Identify the preparation type.
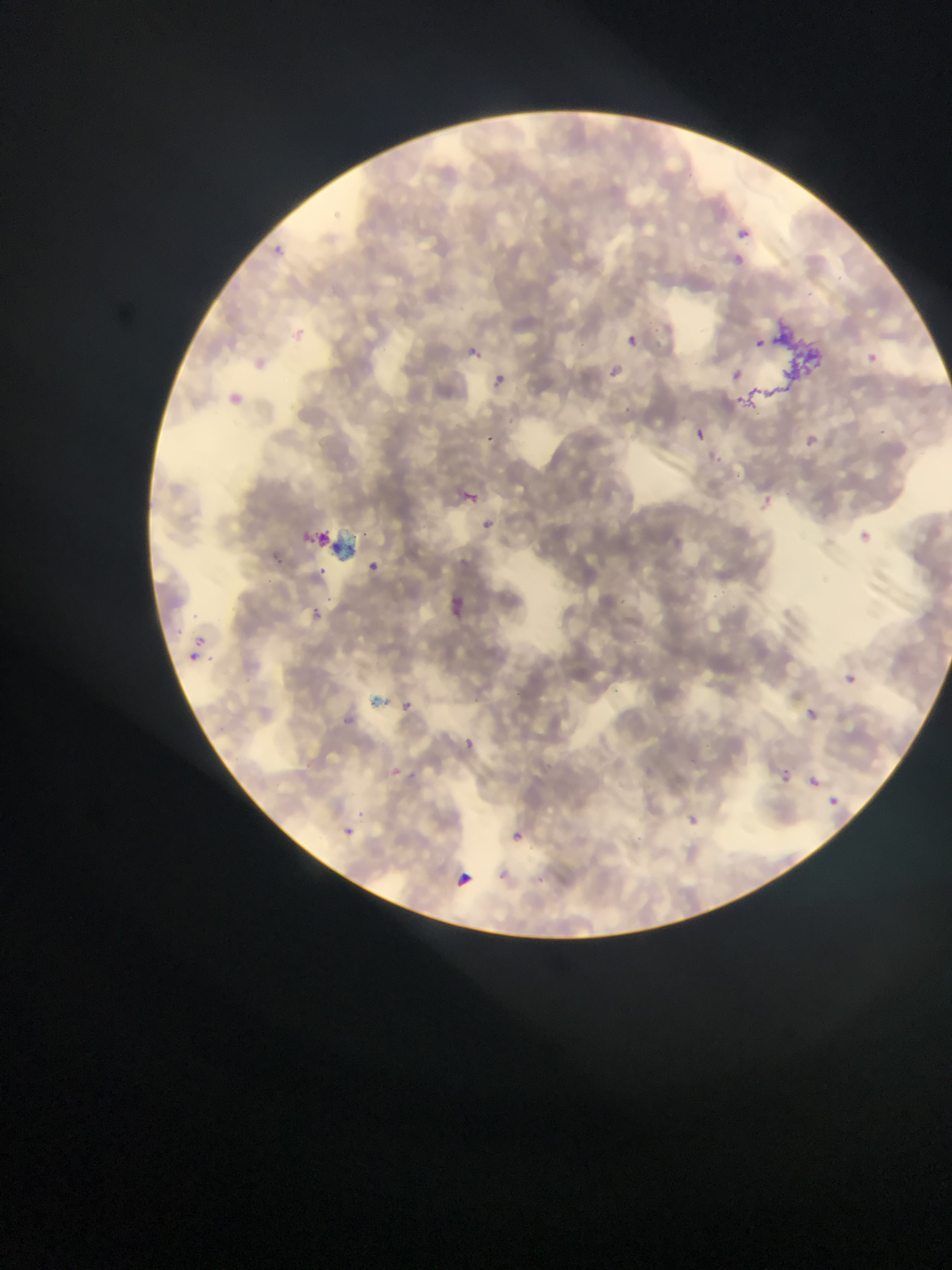

This is a thin smear.

country = Ghana
field of view = single
image size = 952×1270 pixels
capture = mobile-phone photograph through a microscope
malaria parasite locations = approximate bounding boxes as [left, top, right, bottom] in pixels: [733, 224, 753, 244], [267, 246, 283, 259], [735, 254, 751, 271], [302, 318, 314, 340], [627, 329, 640, 349], [466, 343, 482, 359], [862, 349, 886, 371], [605, 360, 636, 386], [257, 362, 276, 376], [492, 373, 507, 388], [225, 382, 248, 413], [688, 421, 710, 452], [785, 421, 836, 449], [481, 429, 498, 448], [457, 485, 485, 505], [748, 501, 780, 526], [474, 517, 501, 531], [858, 528, 872, 546], [262, 534, 287, 573], [319, 561, 343, 587], [373, 566, 383, 579], [446, 588, 467, 619], [311, 608, 331, 625], [188, 634, 207, 647], [192, 655, 207, 673], [843, 666, 862, 688], [400, 689, 416, 709], [798, 701, 817, 721], [335, 710, 359, 727], [453, 732, 482, 753], [386, 766, 404, 780], [781, 770, 793, 781], [807, 776, 818, 787], [831, 798, 840, 806], [679, 806, 703, 826], [509, 823, 530, 854], [335, 824, 363, 838], [453, 869, 475, 891]